Give the position of every malaria parasite and every leukocyte.
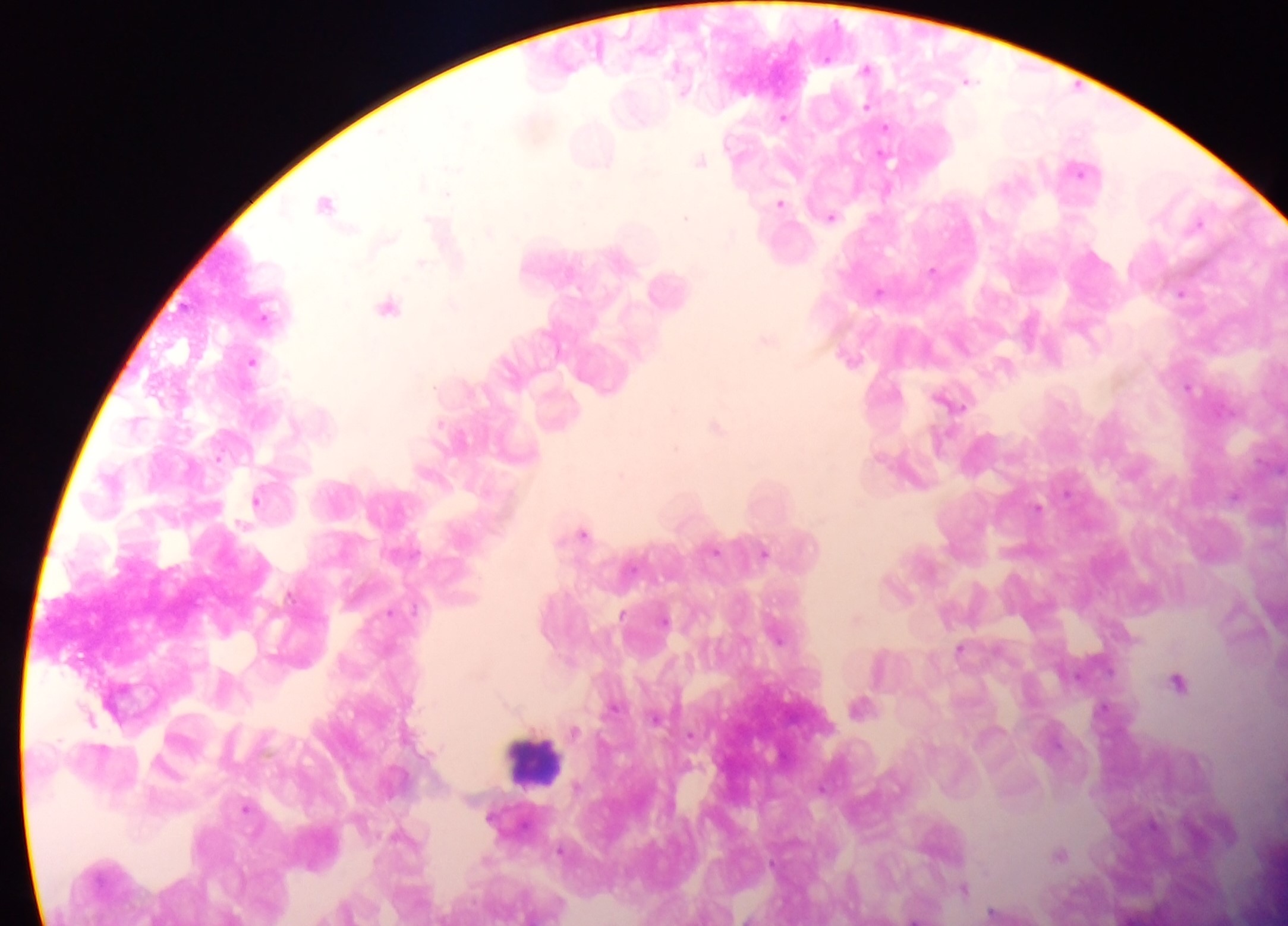

Approximate centers as {x, y} in pixels.
Malaria parasites: {867, 68}, {968, 81}, {867, 105}, {783, 117}, {886, 128}, {700, 159}, {888, 160}, {1078, 169}, {327, 202}, {780, 203}, {686, 217}, {831, 217}, {1197, 223}, {422, 263}, {932, 270}, {879, 291}, {1181, 293}, {388, 306}, {767, 340}, {252, 361}, {1189, 387}, {954, 402}, {717, 426}, {1235, 495}, {257, 501}, {1038, 507}, {584, 533}, {715, 550}, {764, 553}, {392, 612}, {622, 613}, {664, 619}, {779, 639}, {959, 649}, {1178, 682}, {861, 706}, {574, 730}, {246, 807}, {1061, 854}, {964, 888}, {344, 911}.
Leukocytes: {669, 288}, {536, 760}.

preparation: thick blood film
capture: mobile-phone photograph through a microscope
field_of_view: single
image_size: 1288×926 pixels
country: Ghana